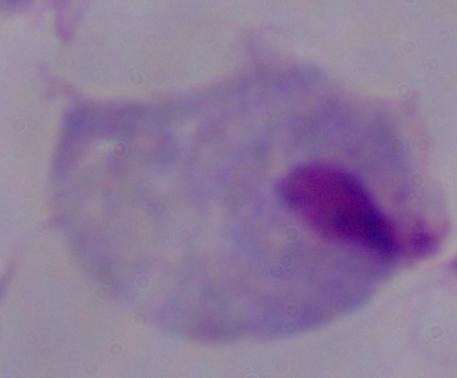
identification = trichomonad
magnification = 1000x
modality = photomicrograph